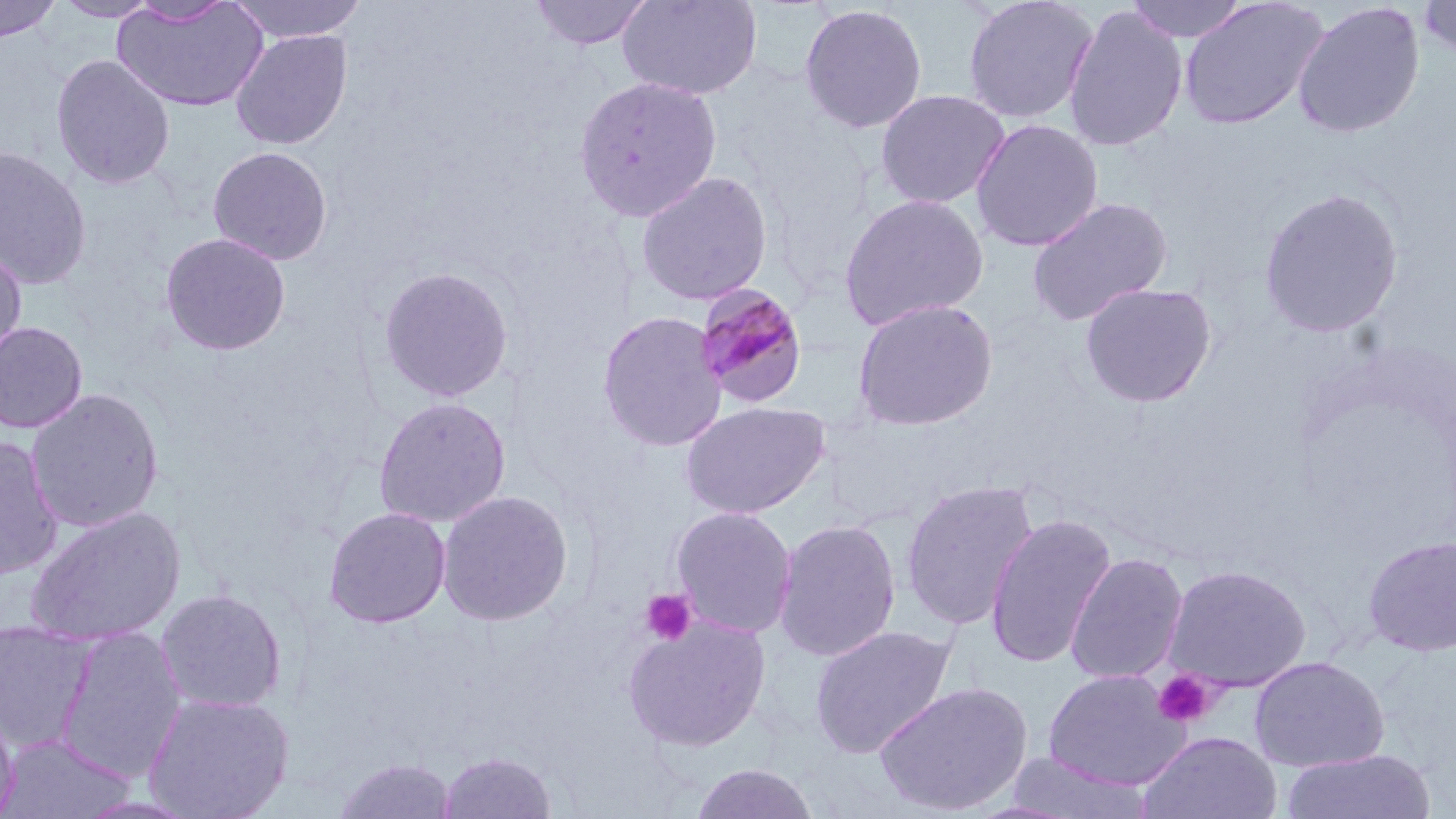

{
  "slide_level_diagnosis": "Plasmodium malariae",
  "field_of_view": "single",
  "platelet_locations": "approximate bounding boxes as [x1, y1, x2, y2] in pixels: [640, 589, 697, 646], [1152, 670, 1219, 729]",
  "magnification": "1000x",
  "plasmodium_malariae_infected_red_blood_cell_locations": "approximate bounding boxes as [x1, y1, x2, y2] in pixels: [695, 282, 809, 409]",
  "modality": "light microscopy",
  "image_size": "1456×819 pixels",
  "uninfected_red_blood_cell_locations": "approximate bounding boxes as [x1, y1, x2, y2] in pixels: [0, 0, 61, 42], [53, 0, 162, 21], [125, 0, 237, 26], [226, 0, 369, 43], [528, 0, 655, 51], [616, 0, 762, 101], [962, 0, 1100, 125], [1126, 0, 1252, 43], [1178, 0, 1328, 130], [1418, 0, 1456, 61], [113, 2, 269, 112], [1292, 2, 1425, 138], [799, 3, 928, 134], [1063, 5, 1188, 152], [230, 29, 352, 150], [50, 54, 175, 190], [573, 76, 723, 222], [875, 89, 1010, 210], [970, 119, 1104, 252], [208, 146, 332, 265], [0, 147, 92, 289], [635, 171, 773, 307], [1259, 187, 1404, 337], [839, 193, 989, 331], [1027, 197, 1173, 327], [161, 232, 291, 356], [0, 248, 27, 368], [379, 265, 513, 402], [1080, 281, 1217, 408], [852, 298, 998, 431], [597, 311, 727, 452], [0, 321, 87, 433], [25, 388, 164, 532], [373, 396, 510, 527], [680, 401, 830, 519], [0, 436, 63, 580], [900, 479, 1039, 631], [437, 490, 574, 627], [670, 505, 797, 638], [25, 506, 185, 646], [324, 506, 450, 628], [984, 514, 1116, 670], [773, 519, 901, 663], [1363, 535, 1456, 655], [1065, 553, 1188, 685], [1162, 565, 1313, 693], [155, 588, 287, 713], [623, 615, 771, 752], [0, 621, 98, 754], [809, 624, 958, 759], [54, 626, 187, 784], [1249, 656, 1389, 772], [1043, 670, 1190, 790], [874, 681, 1033, 817], [143, 692, 294, 819], [0, 704, 19, 819], [1138, 731, 1282, 819], [1, 733, 135, 818], [1282, 749, 1436, 819], [437, 751, 556, 819], [1002, 753, 1153, 818], [332, 758, 457, 818], [689, 763, 821, 819]",
  "preparation": "thin blood film",
  "stain": "May-Grünwald-Giemsa"
}